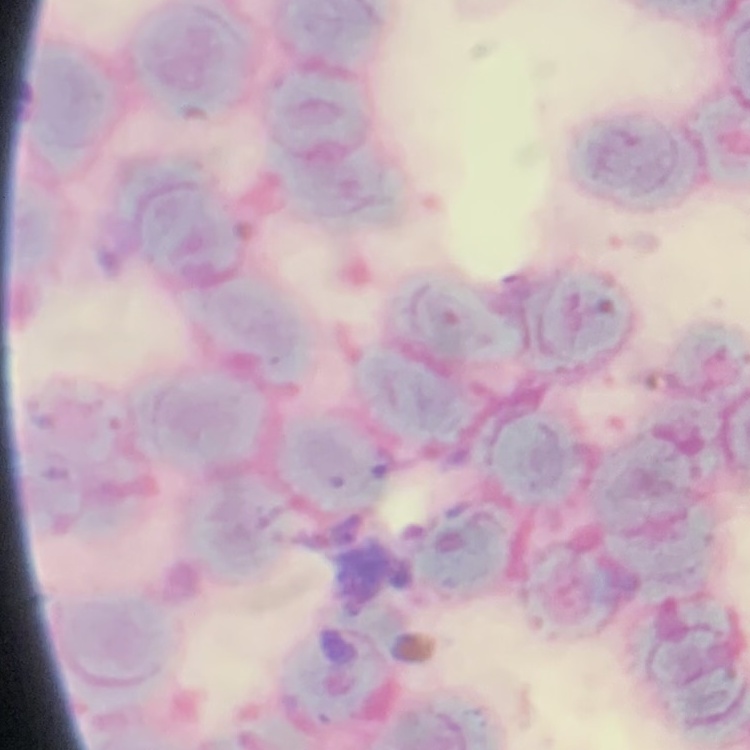

Summary:
  - Erythrocyte morphology: rouleaux formation
  - Image type: square crop of a larger photomicrograph
  - Preparation: thin peripheral smear
  - Stain: Field's or Giemsa